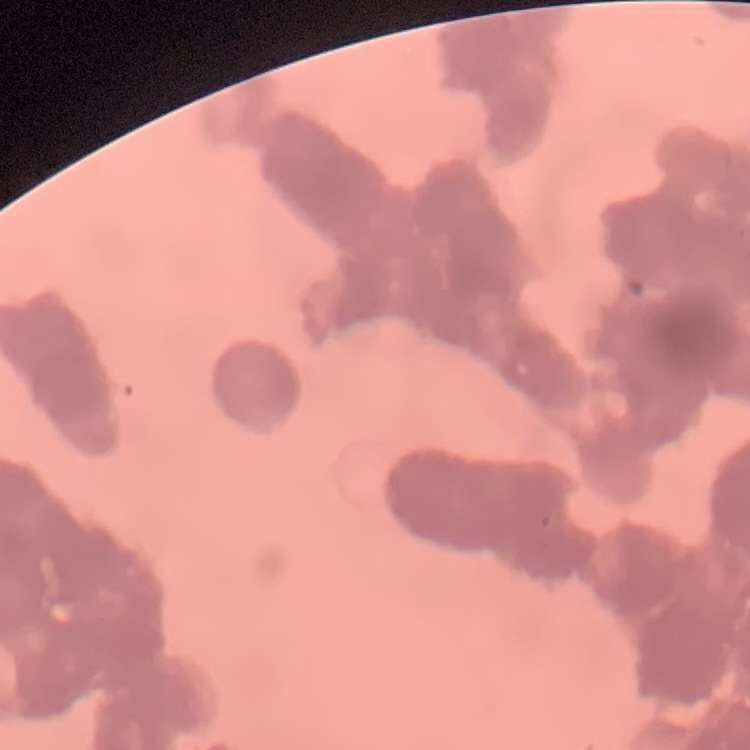

Summary:
  - Erythrocyte morphology: rouleaux formation
  - Preparation: thin blood film
  - Image type: one tile cut from a larger photomicrograph
  - Stain: Field's or Giemsa